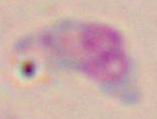

identification = Toxoplasma gondii
magnification = 1000x
modality = micrograph